Give the position of every malaria parasite.
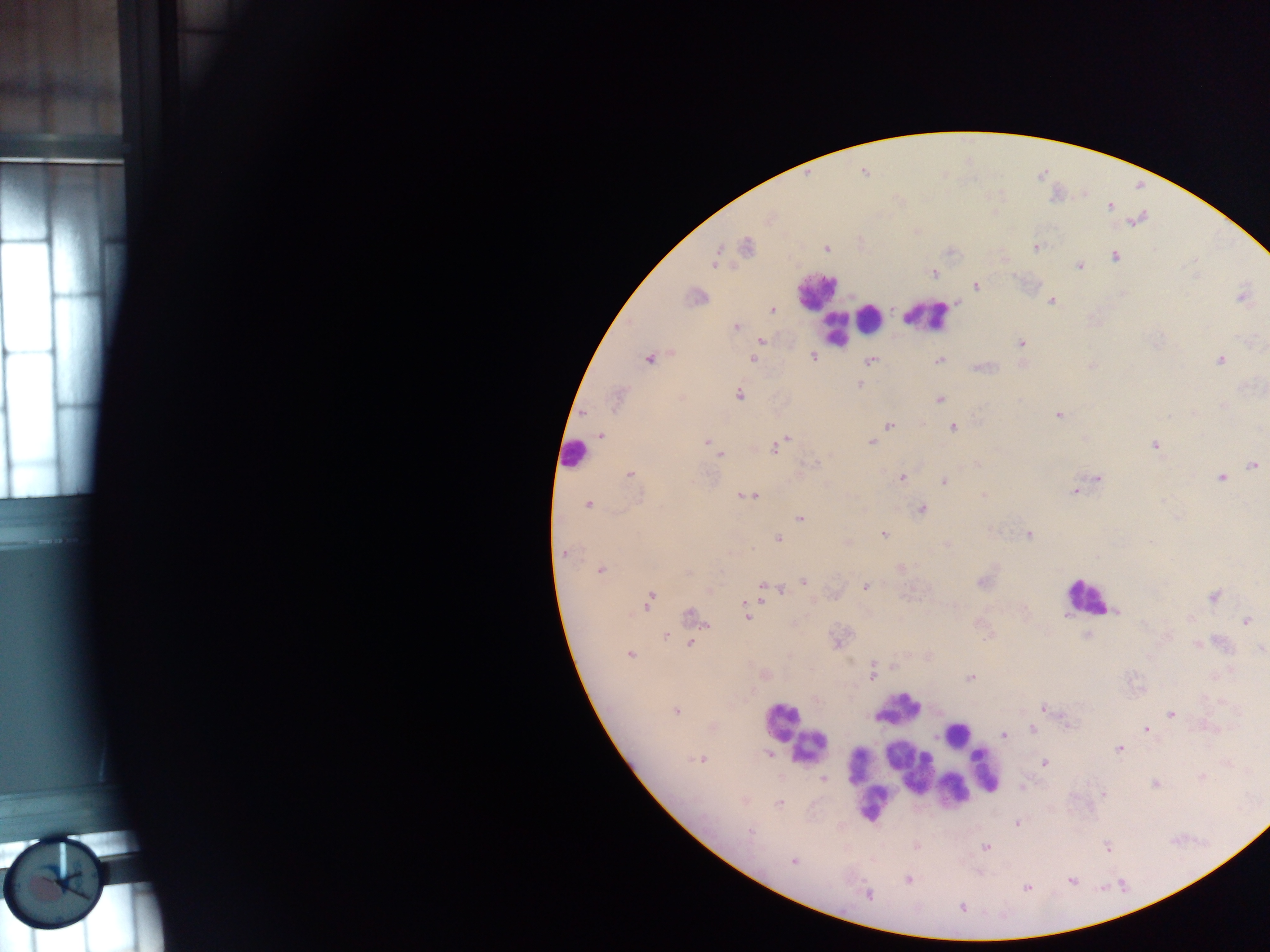

Approximate centers as {x, y} in pixels.
Malaria parasites: {1110, 206}, {746, 247}, {826, 247}, {1035, 247}, {715, 257}, {1116, 257}, {1080, 265}, {933, 273}, {976, 285}, {695, 296}, {1242, 296}, {1051, 301}, {773, 311}, {735, 327}, {760, 340}, {1020, 343}, {813, 356}, {648, 358}, {752, 359}, {1219, 359}, {869, 360}, {939, 360}, {1091, 366}, {980, 367}, {859, 384}, {739, 395}, {617, 398}, {938, 399}, {584, 413}, {1059, 414}, {888, 426}, {952, 427}, {601, 435}, {1084, 439}, {706, 441}, {784, 441}, {870, 441}, {1155, 445}, {775, 447}, {718, 455}, {1252, 465}, {630, 473}, {901, 477}, {1097, 478}, {1221, 478}, {944, 480}, {1081, 487}, {1075, 490}, {746, 496}, {588, 503}, {922, 509}, {799, 518}, {883, 534}, {1027, 534}, {778, 538}, {846, 542}, {947, 545}, {564, 553}, {900, 568}, {600, 569}, {982, 580}, {804, 581}, {865, 586}, {780, 589}, {709, 590}, {767, 590}, {1213, 596}, {648, 600}, {1116, 611}, {748, 615}, {691, 617}, {1246, 620}, {665, 635}, {1088, 635}, {837, 640}, {692, 641}, {1197, 644}, {1259, 649}, {630, 654}, {893, 667}, {872, 673}, {763, 675}, {970, 678}, {1042, 707}, {675, 710}, {1171, 714}, {711, 726}, {1147, 728}, {1032, 729}, {1004, 734}, {1119, 748}, {769, 755}, {700, 759}, {1044, 762}, {822, 778}, {1201, 778}, {1154, 784}, {1021, 787}, {744, 799}, {779, 803}, {1018, 822}, {916, 845}, {985, 847}, {1107, 847}, {793, 861}, {908, 879}, {1071, 880}, {1027, 887}, {867, 894}, {962, 907}.

leukocyte locations = approximate centers as {x, y} in pixels: {816, 291}, {927, 315}, {869, 319}, {846, 323}, {835, 328}, {573, 454}, {1085, 596}, {897, 709}, {782, 720}, {957, 734}, {808, 746}, {893, 753}, {910, 763}, {857, 766}, {985, 770}, {863, 771}, {935, 775}, {952, 789}, {874, 801}
country = Ghana
image size = 1270×952 pixels
field of view = single
preparation = thick blood smear
capture = mobile-phone photograph through a microscope